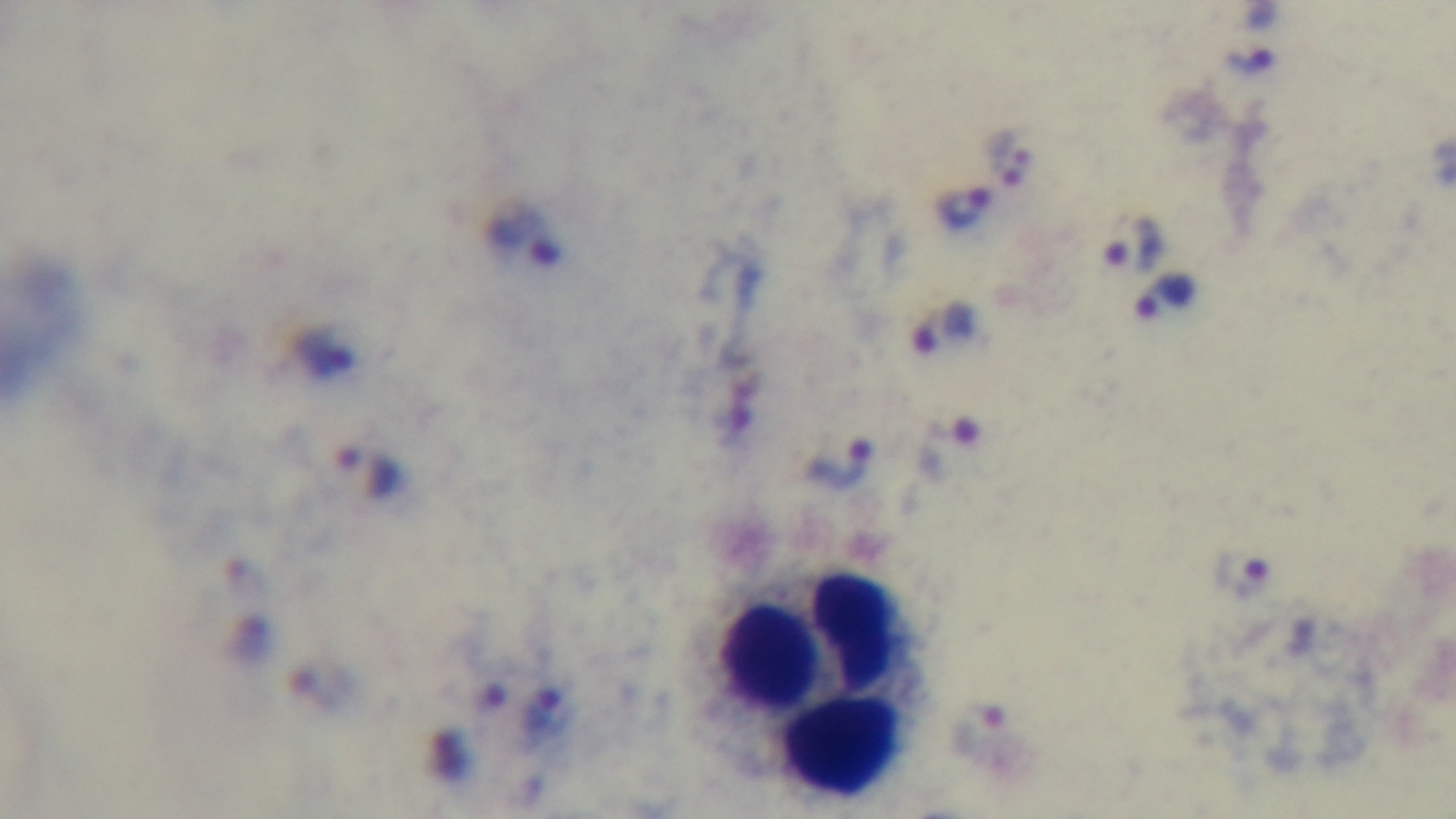
Summary:
  - Objective: 100x oil immersion
  - Preparation: thick
  - Malaria status: positive
  - Field of view: single
  - Capture: mounted 4K digital camera
  - Modality: light microscopy
  - Stain: Giemsa